Name the cell type shown.
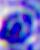
A leukocyte.

Captured at 400x magnification. Micrograph.